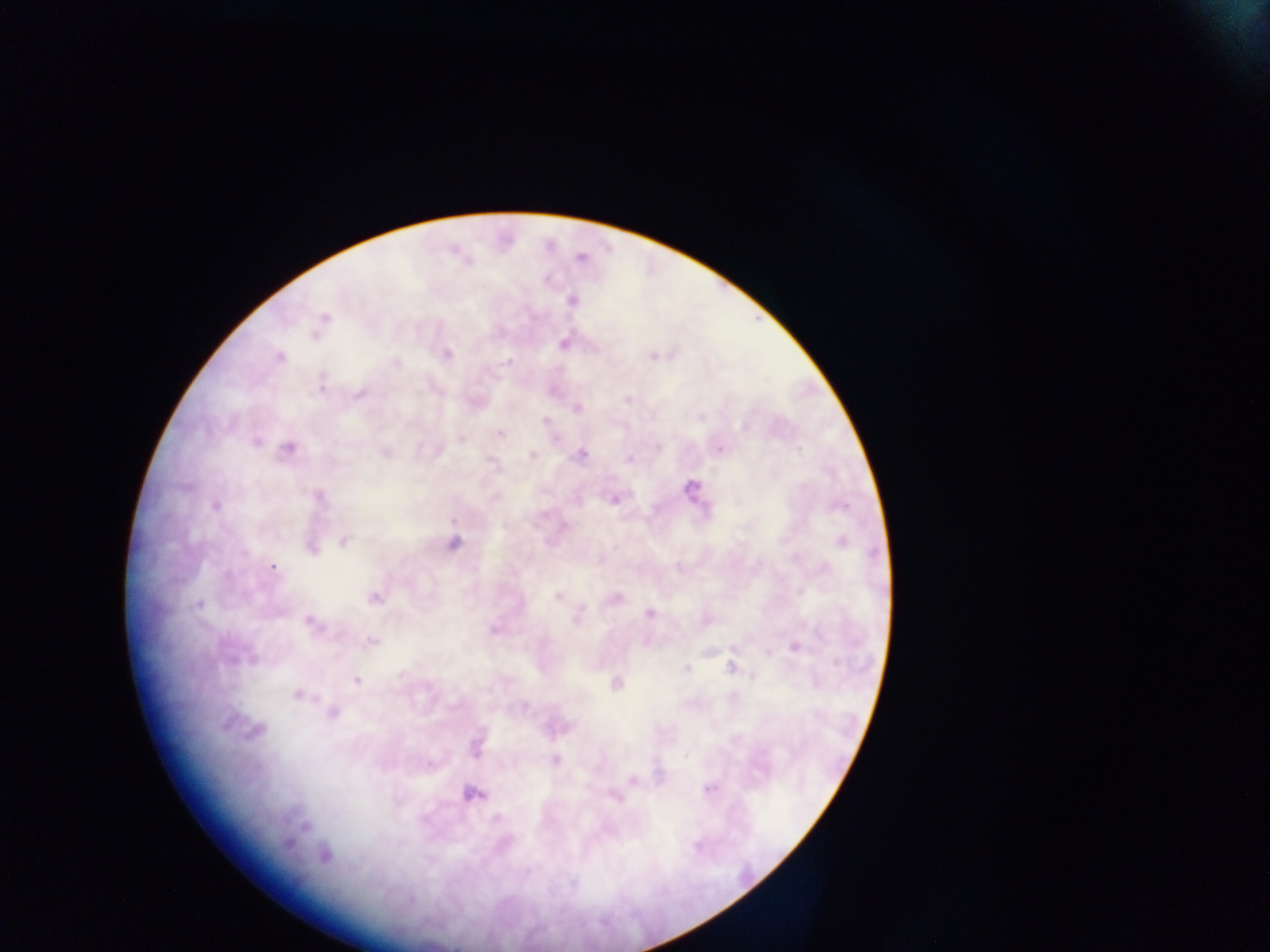

Approximate centers as x y in pixels.
Summary:
  - Plasmodium parasite locations: 581 258; 572 300; 324 318; 564 342; 446 354; 653 356; 279 358; 395 362; 628 398; 475 401; 576 408; 545 422; 500 432; 461 439; 256 440; 718 448; 288 449; 436 450; 384 451; 532 455; 581 455; 491 460; 692 488; 317 496; 613 498; 215 506; 344 540; 840 542; 453 543; 311 546; 272 567; 558 595; 374 598; 615 598; 199 605; 649 612; 311 623; 494 630; 371 642; 795 646; 732 667; 687 669; 356 680; 616 683; 296 694; 332 711; 255 731; 475 743; 554 760; 633 781; 710 788; 472 794; 615 796; 323 854
  - Capture: mobile-phone photograph through a microscope
  - Field of view: single
  - Country: Ghana
  - Preparation: thick blood smear
  - Image size: 1270×952 pixels